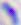
Toxoplasma gondii is seen. 400x magnification. Photomicrograph.